Classify this cell by malaria status.
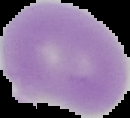
Uninfected.

Summary:
  - Image size: 130×118 pixels
  - Preparation: thin blood smear
  - Image type: cell region segmented out of the field of view; surrounding area masked to black